Assess this cell for malaria.
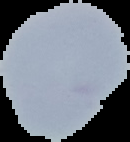

It is uninfected.

Summary:
  - Preparation: thin blood smear
  - Image size: 130×142 pixels
  - Image type: segmented cell region with the area outside set to black